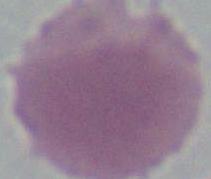

Summary:
  - Identification: erythrocyte
  - Magnification: 1000x
  - Modality: micrograph